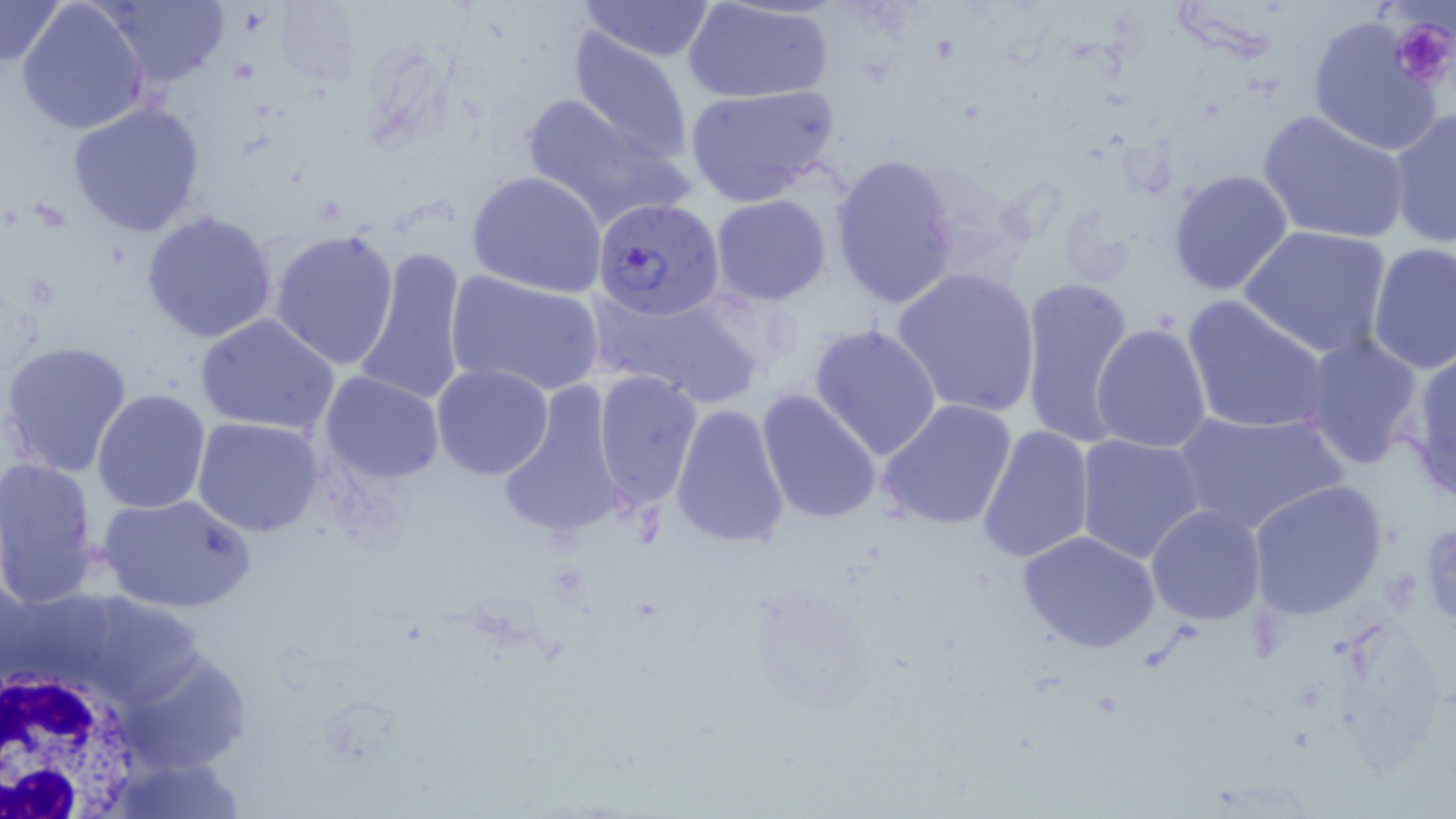
Summary:
  - Coordinate format: approximate bounding boxes as [x1, y1, x2, y2] in pixels
  - White blood cell locations: [0, 655, 157, 817]
  - Uninfected red blood cell locations: [0, 0, 68, 68], [98, 0, 230, 87], [271, 0, 361, 88], [683, 0, 835, 103], [16, 1, 149, 136], [576, 1, 717, 62], [1306, 15, 1443, 156], [564, 27, 695, 167], [684, 84, 841, 209], [520, 92, 684, 229], [68, 100, 206, 236], [1388, 110, 1455, 248], [1258, 111, 1408, 245], [829, 153, 961, 310], [1166, 168, 1296, 297], [467, 170, 606, 298], [710, 195, 833, 305], [141, 209, 278, 343], [1240, 225, 1394, 360], [270, 227, 401, 369], [1366, 243, 1455, 374], [351, 245, 471, 410], [1337, 246, 1451, 465], [890, 266, 1041, 420], [445, 269, 605, 397], [1018, 276, 1135, 450], [589, 285, 762, 409], [1182, 294, 1333, 435], [195, 312, 340, 437], [810, 323, 944, 460], [1091, 323, 1212, 454], [1296, 333, 1427, 471], [1, 340, 134, 479], [1401, 348, 1456, 501], [431, 364, 556, 481], [318, 371, 446, 485], [592, 371, 702, 508], [494, 382, 634, 540], [757, 387, 885, 525], [92, 389, 212, 514], [878, 398, 1018, 531], [670, 402, 791, 548], [1170, 408, 1347, 536], [192, 418, 326, 538], [975, 422, 1095, 565], [1076, 433, 1207, 562], [0, 456, 100, 604], [6, 470, 230, 604], [1245, 479, 1390, 621], [97, 492, 256, 613], [1145, 503, 1268, 626], [1016, 529, 1161, 654]
  - Platelet locations: [1393, 18, 1455, 90]
  - Plasmodium falciparum-infected red blood cell locations: [592, 195, 724, 321]
  - Slide-level diagnosis: Plasmodium falciparum
  - Preparation: thin blood smear
  - Image size: 1456×819 pixels
  - Stain: May-Grünwald-Giemsa
  - Field of view: one of a larger specimen
  - Modality: light microscopy
  - Magnification: 1000x